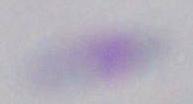

Summary:
  - Magnification: 1000x
  - Identification: Toxoplasma gondii
  - Modality: photomicrograph